Identify the cell.
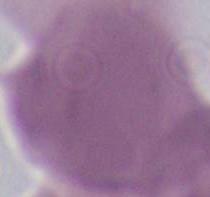

This is an erythrocyte.

magnification = 1000x
modality = photomicrograph